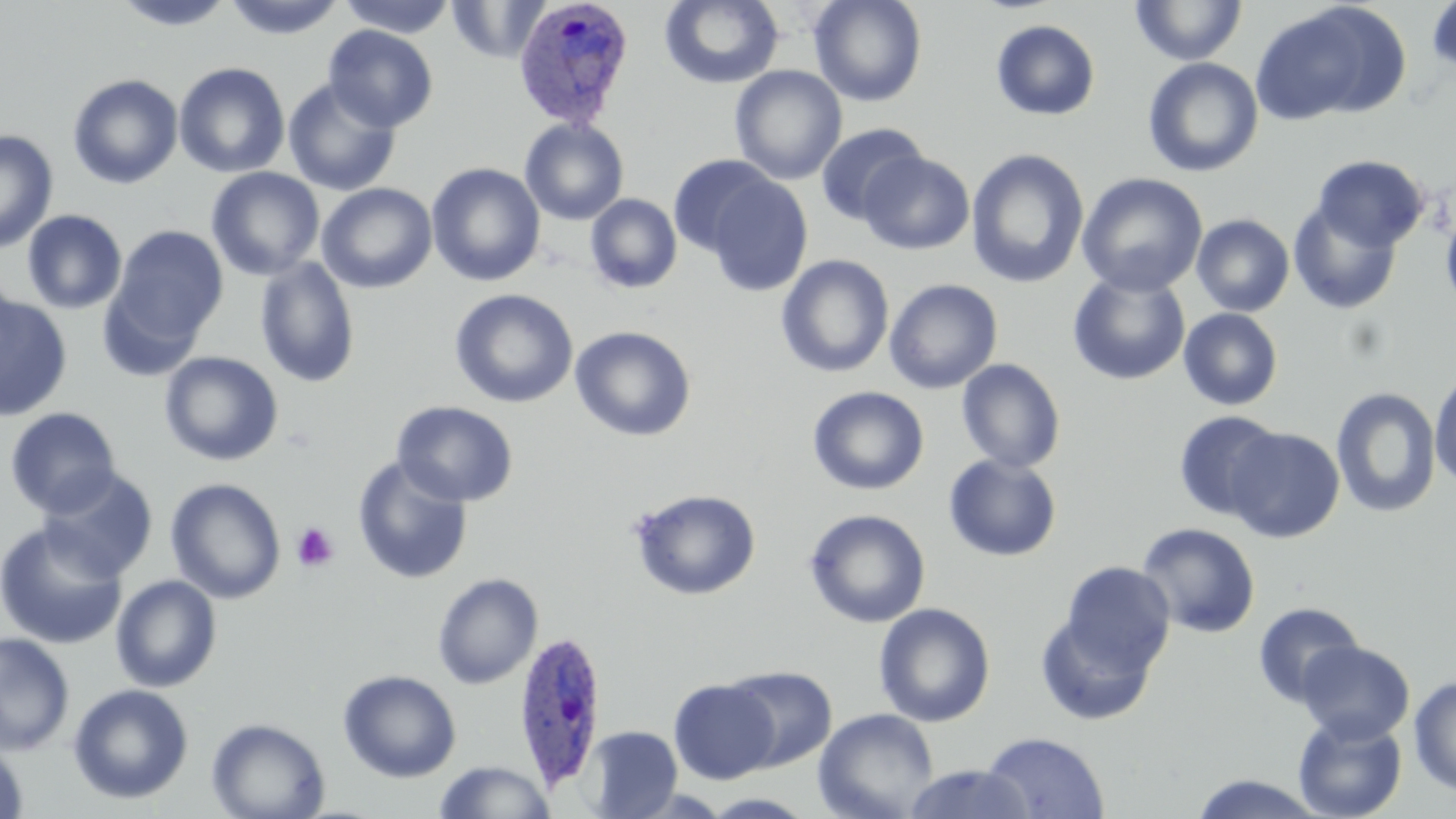
slide_level_diagnosis: Plasmodium ovale
stain: May-Grünwald-Giemsa
uninfected_red_blood_cell_locations: 'approximate bounding boxes as (x1, y1, x2, y2) in pixels: (223, 0, 346, 41), (336, 0, 458, 38), (447, 0, 551, 63), (659, 0, 784, 88), (809, 0, 927, 107), (113, 1, 236, 32), (1129, 1, 1249, 66), (1425, 1, 1456, 76), (1249, 2, 1408, 126), (991, 19, 1100, 121), (323, 25, 438, 132), (1142, 57, 1263, 177), (173, 61, 291, 178), (730, 66, 847, 185), (67, 73, 184, 189), (282, 78, 401, 196), (519, 118, 629, 225), (815, 123, 928, 225), (0, 130, 58, 253), (966, 149, 1089, 289), (860, 151, 974, 255), (1311, 154, 1429, 252), (667, 155, 779, 258), (426, 162, 546, 286), (205, 167, 325, 280), (1077, 172, 1208, 297), (703, 174, 813, 296), (317, 182, 437, 293), (585, 193, 682, 294), (1288, 198, 1403, 315), (1439, 198, 1456, 321), (22, 209, 127, 314), (1191, 213, 1295, 317), (109, 225, 229, 346), (776, 254, 894, 378), (255, 256, 360, 389), (1067, 270, 1191, 386), (0, 274, 21, 381), (884, 278, 1003, 394), (96, 282, 206, 382), (449, 288, 578, 408), (0, 295, 72, 421), (1178, 307, 1284, 411), (570, 326, 696, 442), (159, 351, 283, 466), (956, 358, 1066, 474), (1429, 367, 1456, 490), (807, 386, 930, 495), (1330, 387, 1442, 519), (392, 400, 517, 507), (4, 407, 122, 517), (1172, 411, 1284, 522), (1224, 426, 1345, 543), (943, 454, 1063, 562), (352, 456, 473, 585), (39, 468, 158, 581), (165, 478, 286, 603), (629, 488, 762, 600), (804, 509, 931, 627), (0, 521, 127, 649), (1134, 522, 1261, 638), (1059, 561, 1175, 675), (432, 573, 542, 690), (111, 574, 222, 693), (1252, 601, 1365, 708), (873, 603, 995, 727), (1035, 611, 1159, 726), (0, 632, 74, 755), (1296, 640, 1415, 743), (722, 665, 837, 770), (338, 669, 461, 782), (1408, 674, 1456, 796), (669, 678, 780, 784), (67, 683, 194, 805), (813, 708, 939, 819), (1293, 713, 1408, 819), (206, 717, 329, 819), (582, 725, 682, 819), (980, 731, 1110, 818), (0, 740, 30, 819), (433, 761, 558, 819), (902, 764, 1036, 819), (1187, 773, 1330, 818)'
magnification: 1000x
modality: light microscopy
field_of_view: single
plasmodium_ovale_infected_red_blood_cell_locations: 'approximate bounding boxes as (x1, y1, x2, y2) in pixels: (512, 0, 636, 128), (514, 631, 608, 788)'
preparation: thin blood film
image_size: 1456×819 pixels
platelet_locations: 'approximate bounding boxes as (x1, y1, x2, y2) in pixels: (291, 521, 338, 572)'